Classify this cell by malaria status.
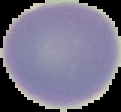
Uninfected.

{
  "image_size": "121×112 pixels",
  "preparation": "thin blood film",
  "image_type": "cell region segmented out of the field of view; surrounding area masked to black"
}